Classify this cell by malaria status.
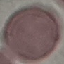
Uninfected.

Thin blood film. Automatically extracted cell patch, resized to 64 × 64 pixels. Photographed with a smartphone camera at the microscope eyepiece. Giemsa stain.